Comment on the morphology of the red blood cells.
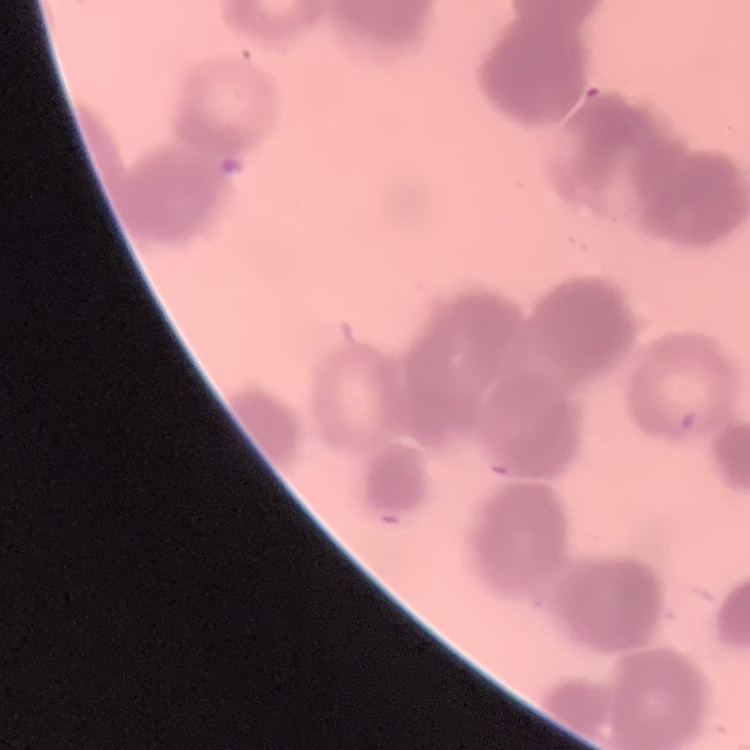

They show rouleaux formation.

Summary:
  - Image type: one tile cut from a larger photomicrograph
  - Stain: Field's or Giemsa
  - Preparation: thin blood smear